Identify the blood parasite species.
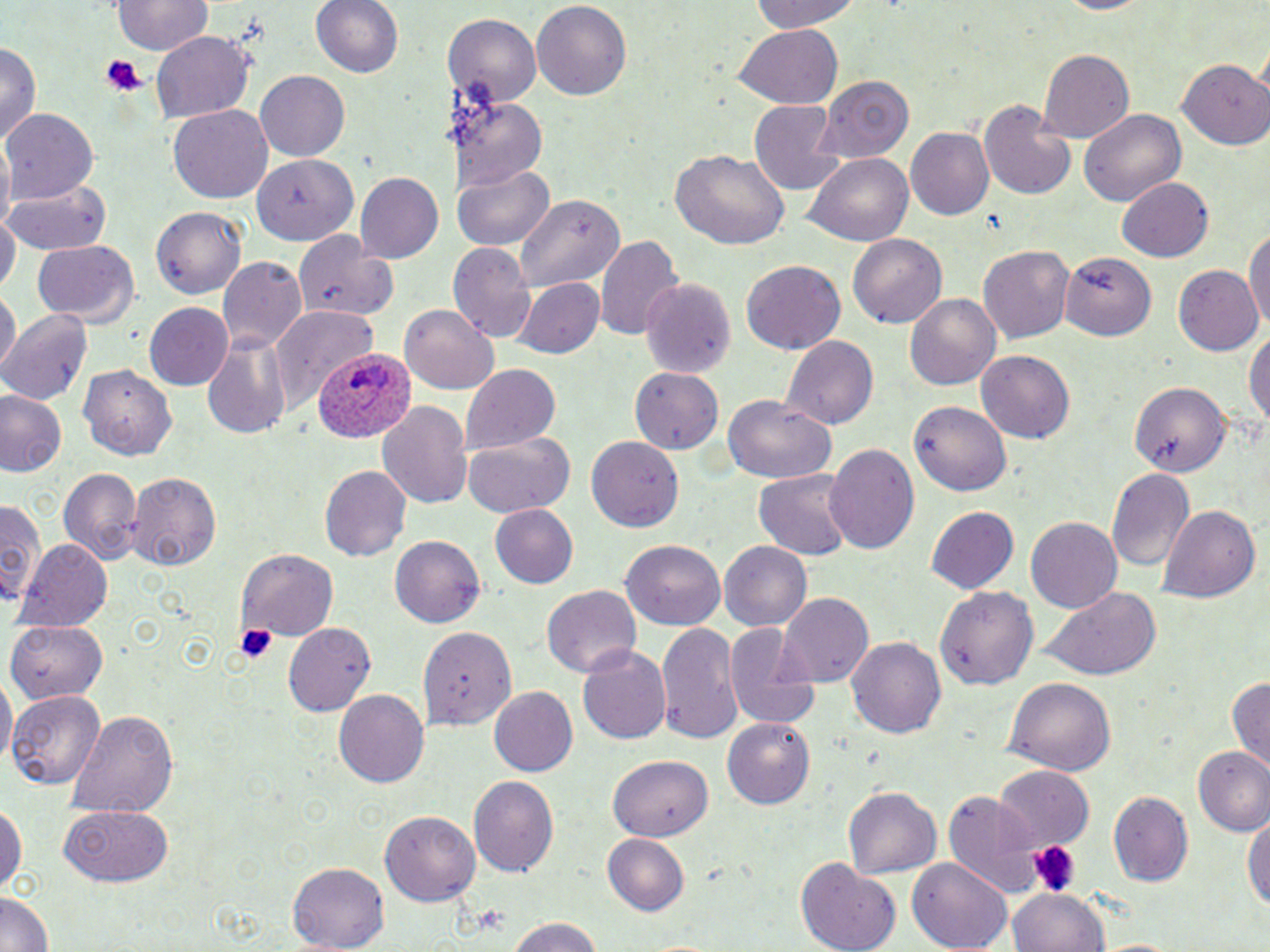

Plasmodium ovale.

Summary:
  - Coordinate format: approximate bounding boxes as named x1/y1/x2/y2 corners in pixels
  - Uninfected red blood cell locations: (x1=310, y1=0, x2=403, y2=82), (x1=531, y1=0, x2=631, y2=100), (x1=743, y1=0, x2=868, y2=32), (x1=112, y1=1, x2=212, y2=56), (x1=446, y1=14, x2=542, y2=105), (x1=734, y1=26, x2=840, y2=106), (x1=152, y1=34, x2=254, y2=121), (x1=0, y1=39, x2=42, y2=148), (x1=1036, y1=48, x2=1135, y2=142), (x1=1179, y1=58, x2=1270, y2=149), (x1=255, y1=69, x2=349, y2=161), (x1=817, y1=76, x2=912, y2=162), (x1=455, y1=93, x2=548, y2=190), (x1=981, y1=97, x2=1077, y2=201), (x1=750, y1=98, x2=844, y2=196), (x1=168, y1=105, x2=273, y2=204), (x1=3, y1=107, x2=99, y2=203), (x1=1080, y1=107, x2=1186, y2=207), (x1=906, y1=127, x2=994, y2=221), (x1=671, y1=148, x2=790, y2=250), (x1=252, y1=153, x2=360, y2=243), (x1=808, y1=154, x2=913, y2=247), (x1=456, y1=167, x2=554, y2=251), (x1=356, y1=171, x2=444, y2=264), (x1=5, y1=174, x2=111, y2=256), (x1=1117, y1=176, x2=1213, y2=263), (x1=515, y1=193, x2=623, y2=294), (x1=151, y1=206, x2=247, y2=300), (x1=1, y1=210, x2=18, y2=300), (x1=1244, y1=221, x2=1270, y2=340), (x1=295, y1=232, x2=397, y2=320), (x1=847, y1=234, x2=945, y2=330), (x1=595, y1=235, x2=683, y2=344), (x1=31, y1=240, x2=140, y2=325), (x1=449, y1=243, x2=537, y2=342), (x1=981, y1=243, x2=1074, y2=345), (x1=1059, y1=253, x2=1155, y2=343), (x1=218, y1=257, x2=307, y2=351), (x1=738, y1=260, x2=845, y2=356), (x1=1173, y1=265, x2=1262, y2=356), (x1=518, y1=277, x2=606, y2=358), (x1=642, y1=278, x2=736, y2=381), (x1=1, y1=289, x2=17, y2=377), (x1=906, y1=293, x2=1000, y2=389), (x1=143, y1=302, x2=235, y2=390), (x1=401, y1=303, x2=499, y2=394), (x1=270, y1=304, x2=374, y2=414), (x1=1, y1=310, x2=92, y2=406), (x1=1247, y1=324, x2=1269, y2=442), (x1=201, y1=334, x2=292, y2=440), (x1=782, y1=334, x2=879, y2=429), (x1=977, y1=348, x2=1074, y2=440), (x1=77, y1=363, x2=177, y2=459), (x1=459, y1=364, x2=560, y2=456), (x1=632, y1=367, x2=722, y2=453), (x1=1127, y1=378, x2=1231, y2=474), (x1=0, y1=389, x2=67, y2=478), (x1=723, y1=396, x2=838, y2=482), (x1=378, y1=399, x2=473, y2=511), (x1=909, y1=400, x2=1011, y2=497), (x1=462, y1=432, x2=575, y2=517), (x1=587, y1=435, x2=686, y2=530), (x1=823, y1=443, x2=921, y2=558), (x1=321, y1=464, x2=413, y2=562), (x1=58, y1=466, x2=143, y2=566), (x1=1105, y1=467, x2=1196, y2=574), (x1=755, y1=469, x2=852, y2=563), (x1=125, y1=472, x2=221, y2=569), (x1=2, y1=498, x2=44, y2=611), (x1=487, y1=504, x2=579, y2=589), (x1=1158, y1=504, x2=1261, y2=602), (x1=927, y1=506, x2=1020, y2=596), (x1=1025, y1=517, x2=1122, y2=616), (x1=390, y1=536, x2=485, y2=631), (x1=17, y1=540, x2=114, y2=628), (x1=719, y1=540, x2=812, y2=629), (x1=622, y1=541, x2=725, y2=631), (x1=235, y1=549, x2=337, y2=644), (x1=937, y1=583, x2=1039, y2=688), (x1=542, y1=585, x2=642, y2=679), (x1=1034, y1=589, x2=1162, y2=680), (x1=778, y1=592, x2=876, y2=686), (x1=5, y1=620, x2=107, y2=701), (x1=658, y1=622, x2=742, y2=742), (x1=726, y1=622, x2=824, y2=730), (x1=283, y1=623, x2=375, y2=715), (x1=419, y1=626, x2=515, y2=732), (x1=846, y1=635, x2=947, y2=738), (x1=578, y1=645, x2=672, y2=747), (x1=1228, y1=674, x2=1270, y2=776), (x1=1005, y1=676, x2=1115, y2=775), (x1=1, y1=678, x2=14, y2=773), (x1=487, y1=686, x2=577, y2=777), (x1=7, y1=689, x2=103, y2=790), (x1=335, y1=689, x2=432, y2=787), (x1=69, y1=708, x2=178, y2=818), (x1=723, y1=713, x2=816, y2=807), (x1=1194, y1=747, x2=1270, y2=835), (x1=609, y1=754, x2=712, y2=842), (x1=994, y1=766, x2=1094, y2=848), (x1=468, y1=774, x2=560, y2=875), (x1=844, y1=786, x2=941, y2=880), (x1=944, y1=792, x2=1047, y2=900), (x1=1107, y1=792, x2=1193, y2=886), (x1=0, y1=796, x2=25, y2=903), (x1=59, y1=806, x2=174, y2=886), (x1=1245, y1=809, x2=1270, y2=914), (x1=379, y1=811, x2=480, y2=905), (x1=601, y1=833, x2=689, y2=916), (x1=798, y1=857, x2=901, y2=952), (x1=909, y1=857, x2=1011, y2=952), (x1=289, y1=864, x2=390, y2=949), (x1=1010, y1=890, x2=1108, y2=952), (x1=0, y1=893, x2=54, y2=951), (x1=504, y1=914, x2=607, y2=951), (x1=1092, y1=938, x2=1188, y2=952)
  - Platelet locations: (x1=100, y1=55, x2=145, y2=95), (x1=235, y1=623, x2=279, y2=664), (x1=1027, y1=842, x2=1076, y2=895)
  - Plasmodium ovale-infected red blood cell locations: (x1=312, y1=347, x2=415, y2=442)
  - Preparation: thin blood film
  - Stain: May-Grünwald-Giemsa
  - Image size: 1270×952 pixels
  - Modality: light microscopy
  - Field of view: single
  - Magnification: 1000x